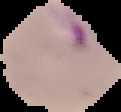 Cell region segmented out of the field of view; the surrounding area is masked to black. Malaria status: parasitized. From a thin blood film. Image is 121×112 pixels.